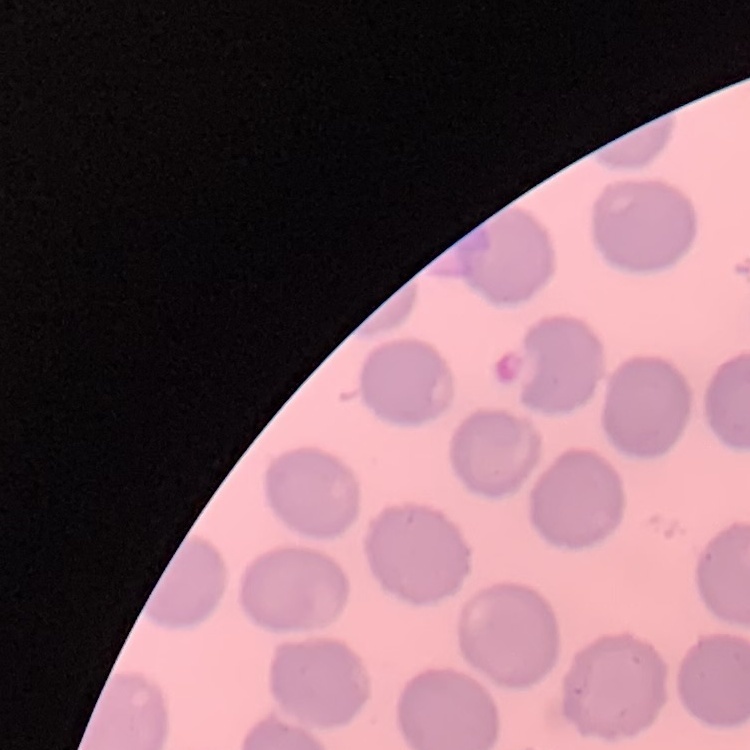
red_blood_cell_morphology: no rouleaux formation
image_type: one tile cut from a larger photomicrograph
preparation: thin blood smear
stain: Field's or Giemsa